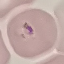
Summary:
  - Malaria status: parasitized
  - Stain: Giemsa
  - Image type: automatically extracted cell patch, resized to 64 × 64 pixels
  - Capture: smartphone camera at the microscope eyepiece
  - Preparation: thin smear